Name the parasite shown.
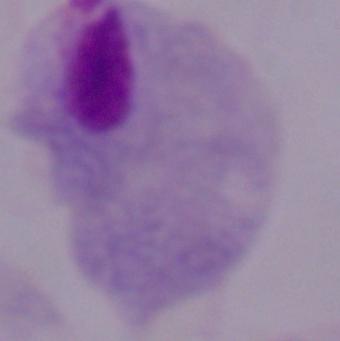

A trichomonad.

modality = micrograph
magnification = 1000x